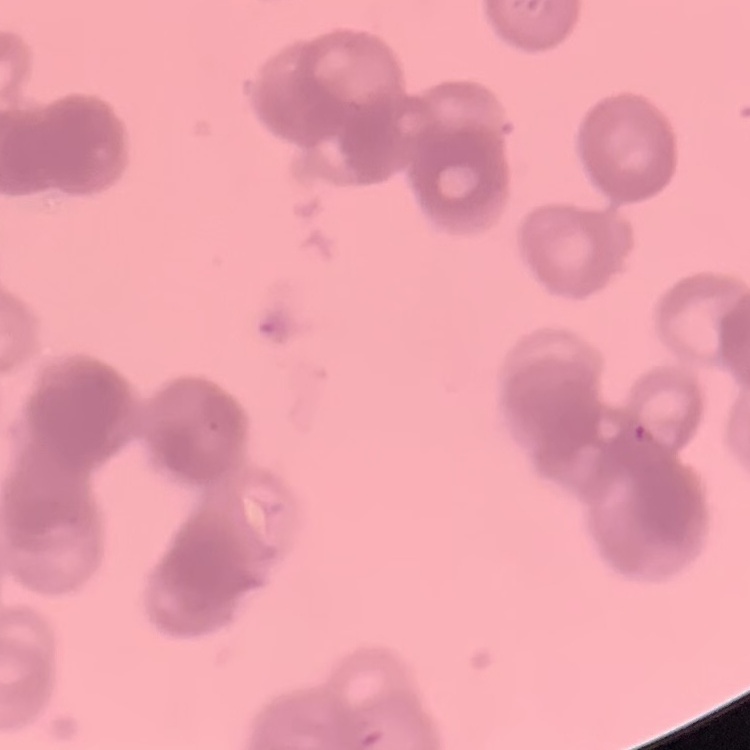 The red blood cells exhibit rouleaux formation. Field's or Giemsa stain. Square crop of a larger photomicrograph. Thin blood smear.